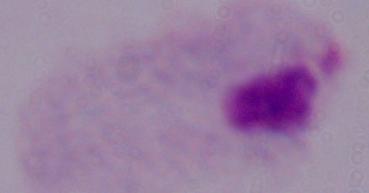 A trichomonad is shown. 1000x magnification. Micrograph.